State the blood parasite species.
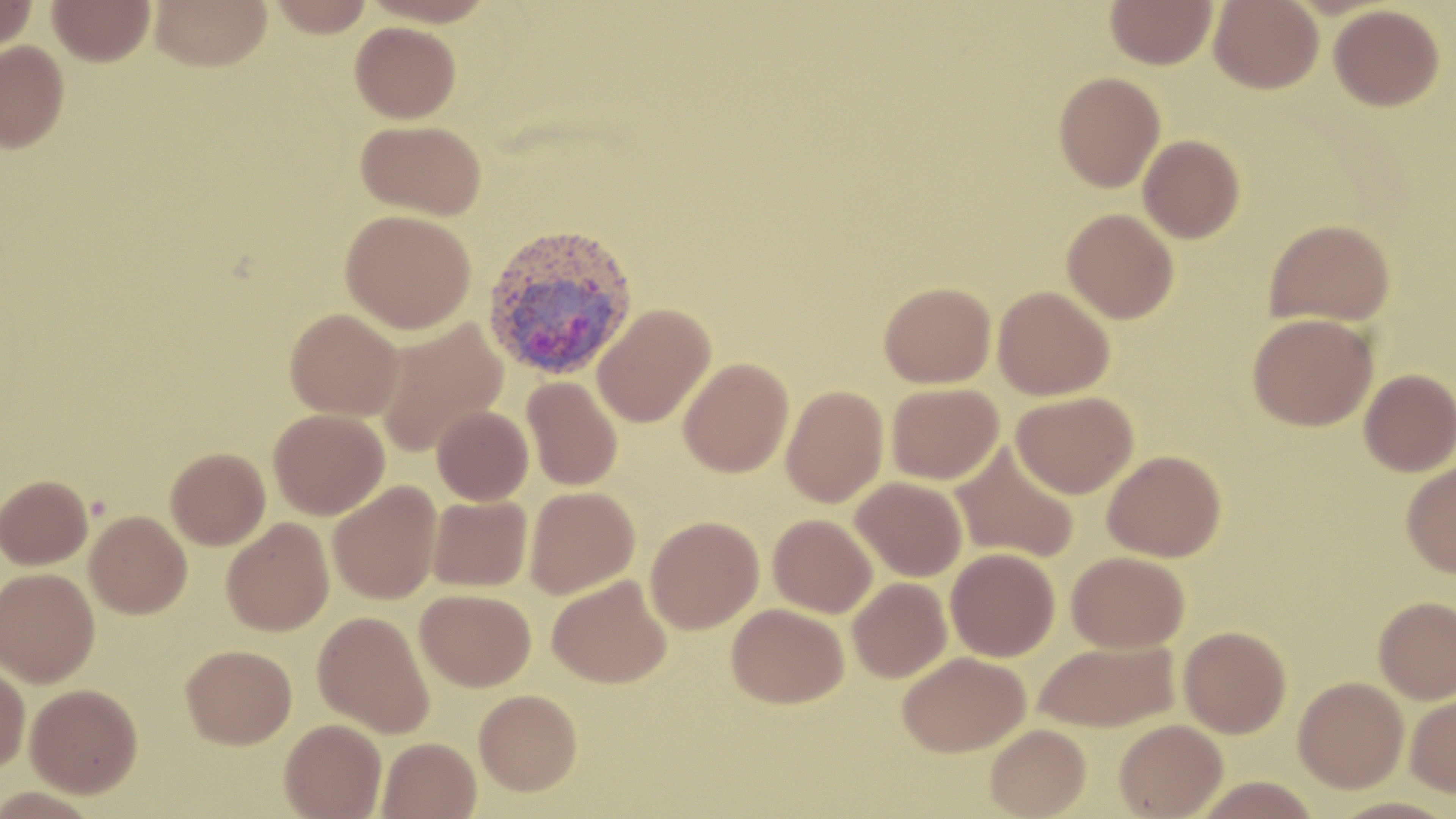
Plasmodium vivax.

Approximate bounding boxes as [x1, y1, x2, y2] in pixels. Plasmodium vivax-infected red blood cell locations: [481, 221, 639, 380]. Uninfected red blood cell locations: [0, 0, 37, 55], [48, 0, 155, 66], [150, 0, 271, 70], [268, 0, 375, 37], [1106, 0, 1218, 69], [1209, 0, 1323, 93], [1329, 4, 1445, 111], [350, 21, 460, 123], [0, 40, 69, 152], [1053, 71, 1165, 192], [356, 119, 487, 220], [1138, 134, 1245, 243], [1062, 208, 1179, 323], [340, 209, 476, 334], [1264, 218, 1396, 327], [879, 282, 996, 388], [993, 286, 1115, 400], [592, 303, 716, 427], [285, 307, 403, 421], [1247, 313, 1378, 431], [373, 318, 508, 458], [678, 357, 793, 477], [1359, 369, 1456, 476], [522, 376, 623, 491], [886, 383, 1004, 485], [781, 385, 888, 508], [1011, 391, 1139, 498], [432, 405, 533, 505], [268, 408, 389, 519], [950, 441, 1080, 564], [166, 447, 271, 550], [1102, 450, 1226, 562], [1400, 461, 1456, 577], [1, 475, 93, 569], [851, 476, 968, 581], [328, 480, 442, 604], [524, 486, 640, 599], [427, 495, 533, 592], [85, 510, 192, 618], [768, 513, 877, 617], [645, 516, 764, 634], [222, 517, 334, 636], [946, 548, 1060, 662], [1066, 551, 1189, 653], [0, 568, 100, 687], [547, 574, 672, 688], [848, 577, 952, 682], [415, 588, 536, 691], [1374, 596, 1456, 704], [727, 602, 849, 708], [312, 610, 435, 738], [1178, 625, 1292, 738], [1033, 639, 1179, 732], [181, 644, 297, 748], [897, 651, 1030, 757], [0, 663, 30, 773], [1293, 676, 1409, 792], [25, 683, 143, 797], [474, 688, 582, 795], [1405, 692, 1456, 797], [280, 718, 386, 818], [1114, 719, 1227, 818], [985, 723, 1091, 818], [378, 737, 481, 819], [1192, 776, 1321, 819]. Image is 1456×819 pixels. One field of a larger specimen. Optical microscopy. Captured at 1000x magnification. Thin blood smear. May-Grünwald-Giemsa-stained preparation.